Locate every leukocyte (white blood cell).
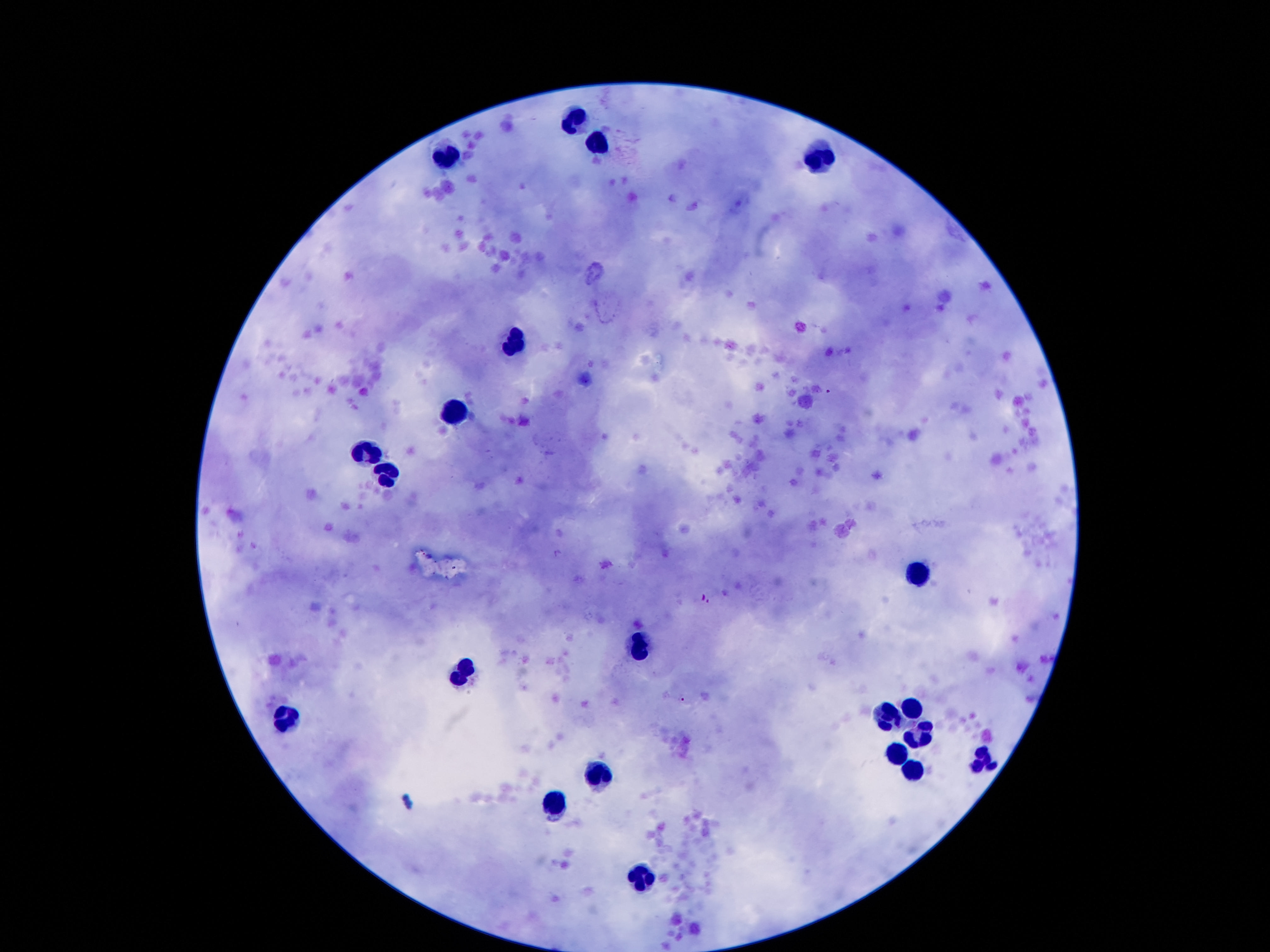

Approximate centers as (x, y) in pixels.
Leukocytes: (578, 121), (601, 145), (821, 154), (446, 156), (506, 341), (453, 414), (362, 455), (390, 475), (920, 576), (638, 647), (459, 675), (912, 707), (884, 714), (287, 720), (922, 737), (896, 755), (980, 761), (599, 772), (916, 772), (556, 804), (642, 884).

Summary:
  - Magnification: 100x
  - Preparation: thick peripheral-blood smear
  - Patient malaria status: negative
  - Stain: Giemsa
  - Image size: 1270×952 pixels
  - Field of view: one from this slide
  - Capture: smartphone camera through the microscope eyepiece